Classify this cell by malaria status.
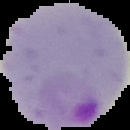
Parasitized.

Summary:
  - Image size: 130×130 pixels
  - Image type: segmented cell region on a black background
  - Preparation: thin blood smear